Point out each leukocyte.
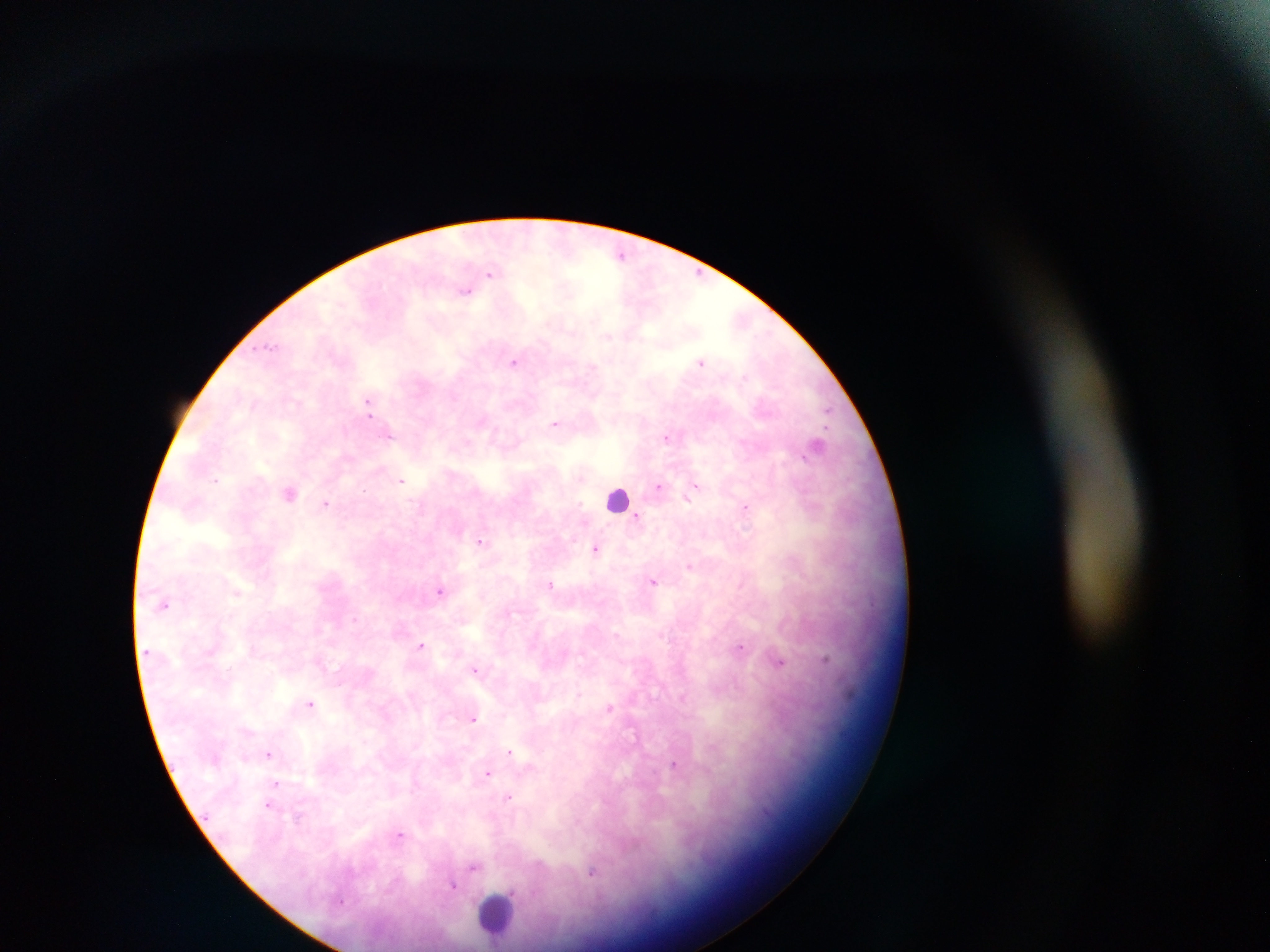

Approximate centers as x y in pixels.
Leukocytes: 617 498; 497 916.

Malaria parasite locations: 490 274; 699 277; 466 292; 516 362; 700 362; 366 407; 827 409; 555 423; 667 438; 817 444; 214 478; 402 480; 695 484; 661 487; 290 494; 690 495; 326 504; 744 508; 638 518; 482 543; 595 548; 689 567; 655 582; 552 584; 440 591; 237 594; 422 645; 741 645; 828 659; 782 661; 474 669; 311 702; 609 708; 474 718; 246 730; 510 752; 268 754; 675 768; 488 773; 275 782; 415 783; 509 797; 267 804; 299 817; 401 834; 474 867; 593 873; 453 884. Collected in Ghana. Image is 1270×952 pixels. Thick blood film. Photographed through a microscope with a mobile-phone camera. One field of view.